Locate every blood parasite and identify its species.
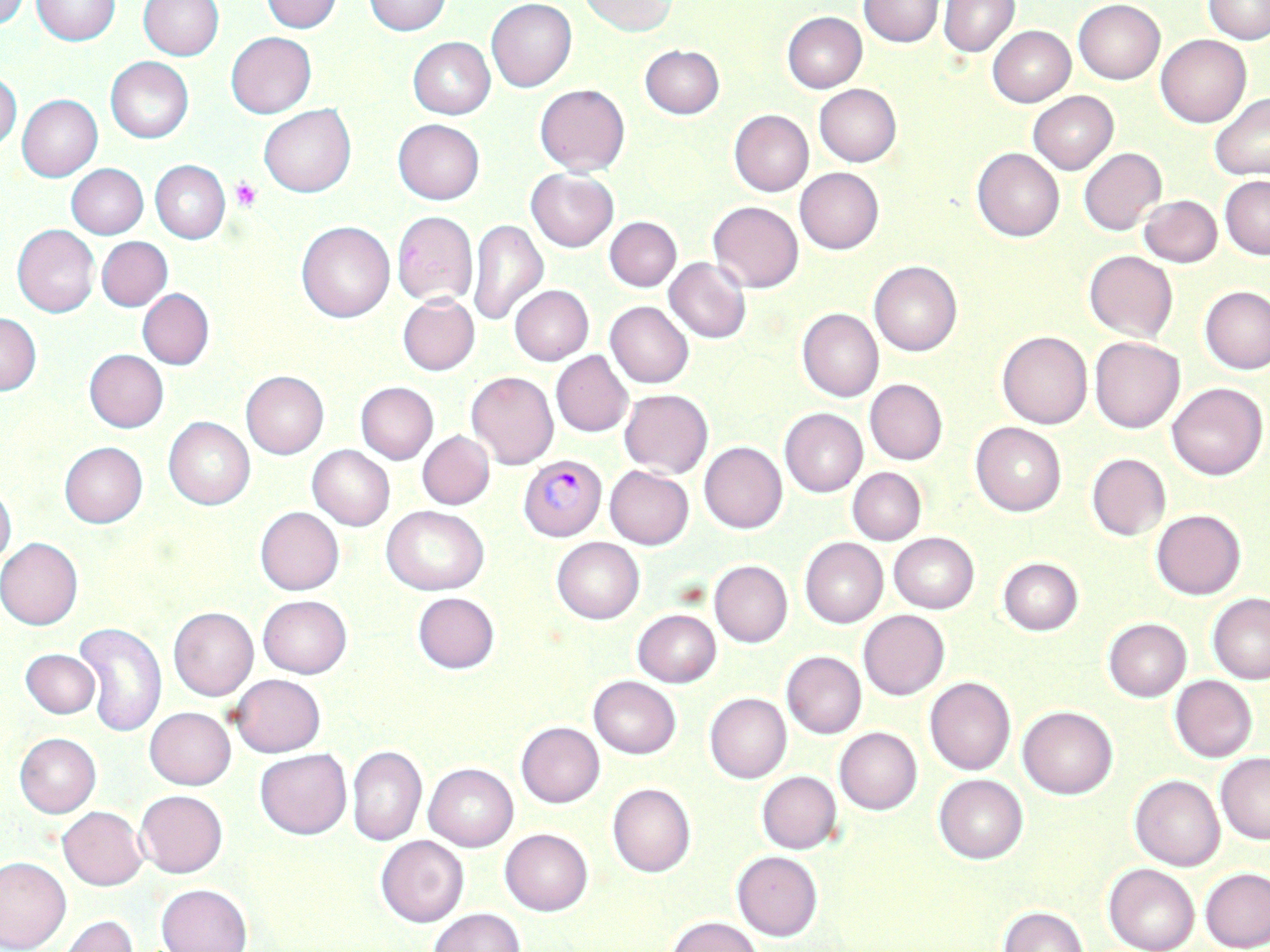

Approximate bounding boxes as [x1, y1, x2, y2] in pixels.
Plasmodium falciparum-infected red blood cells: [518, 455, 606, 541].
No Plasmodium ovale, Plasmodium malariae, Plasmodium vivax, Babesia divergens, or Trypanosoma brucei observed.

slide-level diagnosis = Plasmodium falciparum
preparation = thin blood film
uninfected red blood cell locations = approximate bounding boxes as [x1, y1, x2, y2] in pixels: [30, 0, 122, 46], [262, 0, 342, 33], [486, 0, 576, 92], [583, 0, 675, 36], [858, 0, 944, 48], [1202, 0, 1270, 42], [0, 1, 26, 32], [137, 1, 223, 60], [364, 1, 452, 35], [1073, 1, 1165, 84], [939, 2, 1018, 56], [782, 12, 866, 93], [988, 26, 1076, 107], [226, 32, 317, 118], [1156, 35, 1251, 127], [407, 37, 495, 119], [640, 46, 724, 119], [105, 57, 194, 143], [0, 72, 22, 150], [534, 84, 630, 176], [814, 84, 901, 166], [1028, 91, 1119, 174], [1209, 92, 1270, 180], [16, 95, 103, 182], [259, 106, 355, 197], [729, 110, 814, 196], [393, 119, 485, 204], [973, 147, 1064, 241], [1078, 148, 1166, 235], [150, 160, 230, 243], [65, 164, 148, 239], [795, 167, 884, 254], [526, 170, 619, 252], [1220, 176, 1270, 259], [1138, 194, 1223, 267], [708, 201, 804, 293], [392, 211, 477, 306], [604, 216, 681, 292], [468, 219, 548, 327], [296, 221, 395, 323], [12, 224, 100, 318], [97, 236, 172, 311], [1084, 250, 1177, 342], [665, 257, 751, 344], [870, 261, 962, 357], [509, 285, 593, 364], [1201, 287, 1270, 374], [138, 289, 214, 369], [398, 293, 480, 376], [604, 302, 694, 388], [797, 307, 884, 402], [1, 314, 41, 394], [997, 331, 1092, 429], [1091, 337, 1186, 433], [83, 350, 169, 432], [550, 351, 633, 437], [241, 370, 329, 460], [466, 371, 559, 469], [864, 378, 948, 465], [355, 382, 438, 464], [1167, 382, 1267, 480], [619, 389, 712, 478], [779, 408, 867, 497], [163, 417, 255, 510], [971, 422, 1066, 516], [417, 431, 494, 509], [59, 441, 148, 528], [699, 442, 787, 534], [308, 446, 395, 530], [1087, 453, 1171, 541], [604, 465, 694, 549], [847, 467, 925, 544], [0, 482, 16, 567], [381, 505, 489, 595], [255, 506, 344, 595], [1151, 509, 1246, 600], [889, 532, 979, 613], [552, 537, 645, 623], [801, 537, 888, 628], [0, 539, 83, 630], [998, 557, 1084, 635], [709, 559, 792, 647], [412, 592, 499, 673], [1208, 594, 1270, 684], [258, 595, 352, 677], [168, 607, 258, 701], [633, 609, 720, 686], [857, 609, 950, 700], [1103, 618, 1191, 702], [75, 622, 167, 738], [21, 649, 99, 719], [781, 650, 866, 739], [232, 674, 325, 756], [1169, 675, 1258, 762], [589, 677, 681, 759], [926, 677, 1016, 776], [705, 692, 792, 784], [1018, 706, 1117, 799], [145, 707, 235, 789], [516, 721, 605, 808], [835, 727, 922, 815], [15, 733, 101, 818], [347, 745, 426, 847], [255, 749, 352, 838], [1216, 753, 1270, 844], [424, 762, 518, 851], [756, 771, 841, 854], [933, 775, 1028, 864], [1130, 775, 1225, 870], [608, 782, 696, 878], [135, 789, 227, 878], [58, 807, 148, 890], [499, 828, 592, 916], [377, 835, 468, 927], [731, 850, 823, 940], [0, 857, 72, 950], [1104, 864, 1200, 952], [1200, 867, 1270, 952], [156, 883, 251, 952], [998, 906, 1088, 952], [429, 908, 524, 951], [58, 916, 138, 952], [668, 916, 763, 952]
stain = May-Grünwald-Giemsa
magnification = 1000x
platelet locations = approximate bounding boxes as [x1, y1, x2, y2] in pixels: [233, 178, 261, 210]
image size = 1270×952 pixels
field of view = one of a larger specimen
modality = optical microscopy